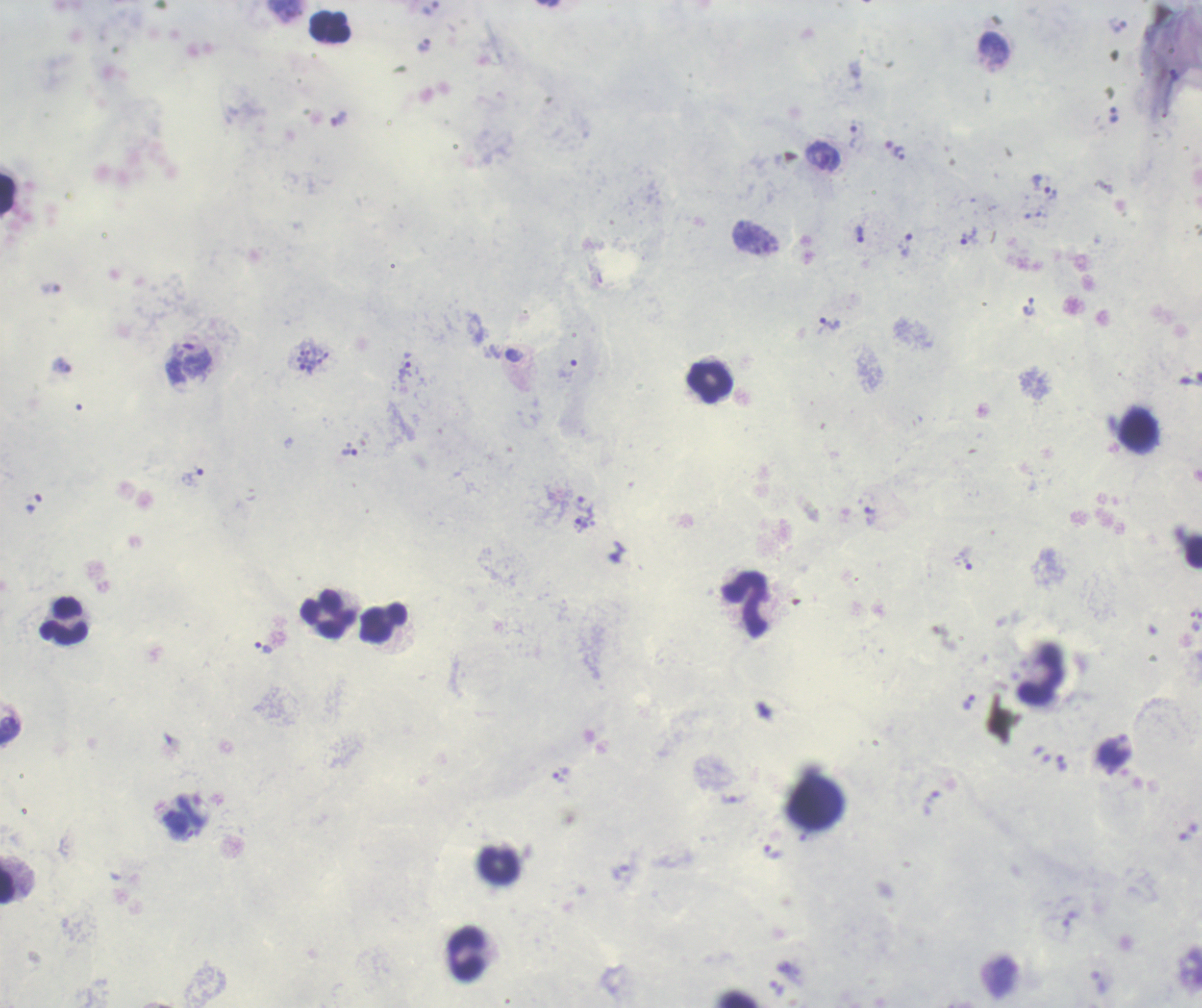

coordinate format = approximate centers as {x, y} in pixels
trophozoite locations = {423, 45}, {1113, 114}, {854, 136}, {894, 147}, {822, 155}, {1042, 185}, {859, 233}, {968, 236}, {907, 244}, {830, 324}, {189, 363}, {566, 368}, {404, 371}, {349, 452}, {191, 478}, {582, 503}, {869, 516}, {583, 525}, {263, 647}, {968, 701}, {561, 776}, {772, 852}
schizont locations = {312, 361}
leukocyte locations = {331, 27}, {8, 196}, {711, 382}, {1136, 429}, {1193, 553}, {746, 606}, {328, 615}, {65, 622}, {384, 624}, {1040, 677}, {500, 866}, {7, 886}, {468, 954}
life-cycle stages observed = trophozoite, schizont
coloration quality = good
result = Plasmodium parasites identified
preparation = thick blood smear
context = previously used in an actual diagnosis
field of view = single
magnification = 100x
stain = Romanowsky
image size = 1202×1008 pixels
background quality = good